Describe the morphology of the red blood cells.
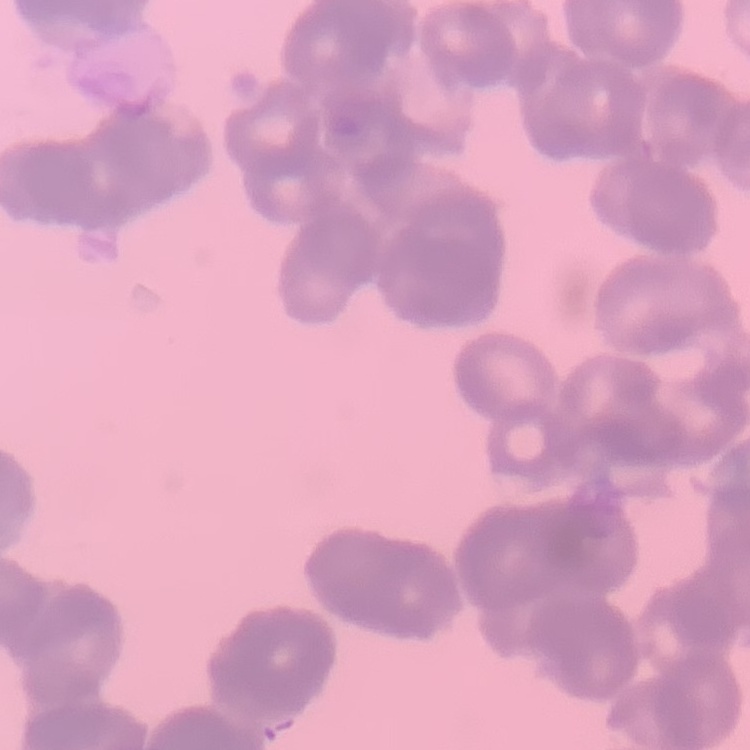
They show rouleaux formation.

image type = one tile cut from a larger photomicrograph
preparation = thin blood smear
stain = Field's or Giemsa